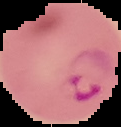
Result: Plasmodium parasites identified. Image is 121×127 pixels. From a thin blood film. Cell region segmented out of the field of view; the surrounding area is masked to black.